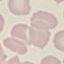
malaria status = uninfected
image type = automatically extracted cell patch, resized to 64 × 64 pixels
capture = smartphone camera at the microscope eyepiece
stain = Giemsa
preparation = thin blood smear